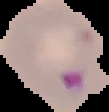
image_type: segmented cell region on a black background
result: malaria parasites identified
image_size: 109×112 pixels
preparation: thin blood smear